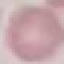
Summary:
  - Malaria status: uninfected
  - Stain: Giemsa
  - Capture: smartphone through the microscope eyepiece
  - Image type: cell patch, automatically extracted from a larger field of view and resized to 64 × 64 pixels
  - Preparation: thin blood film